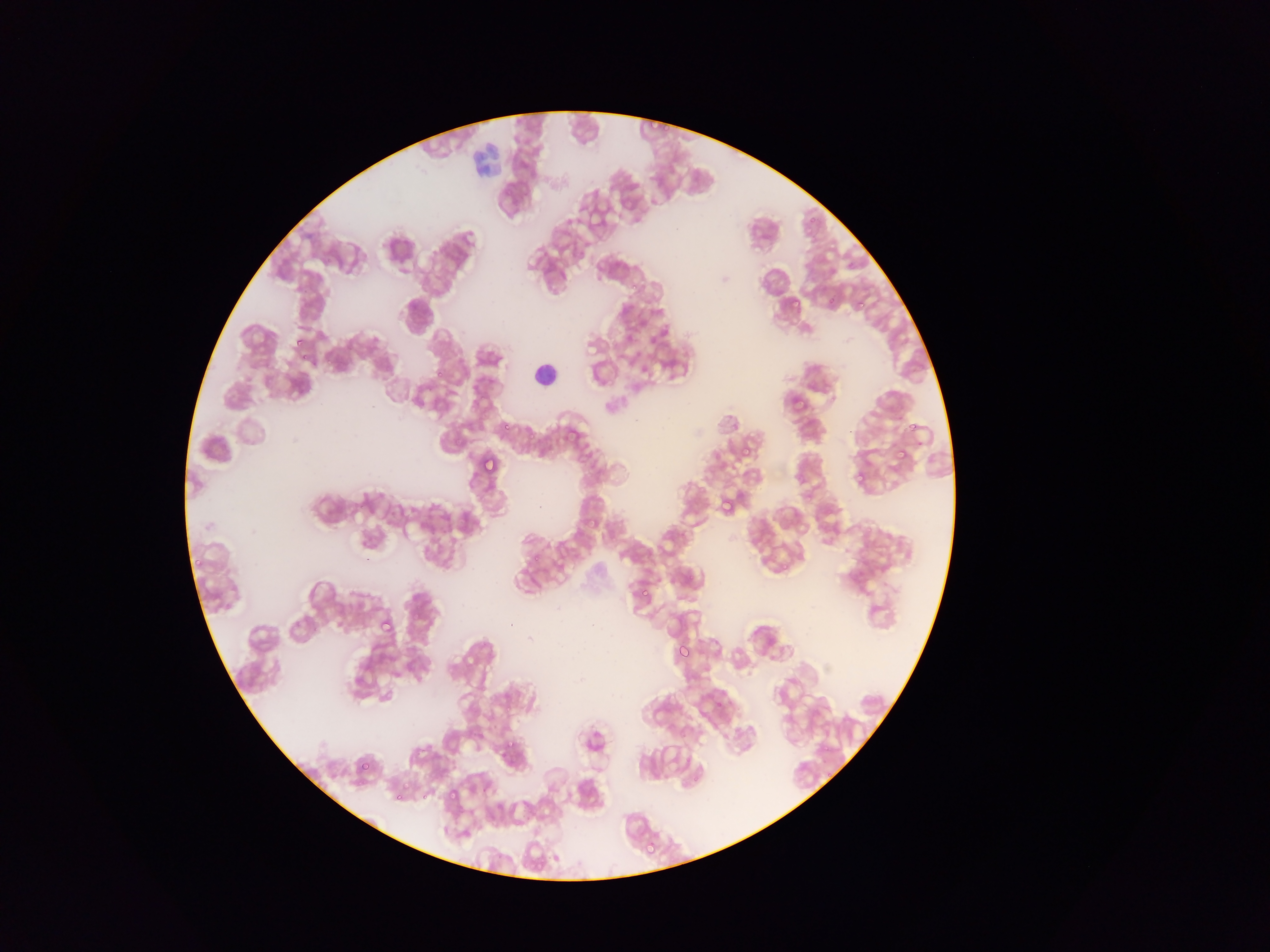
image size = 1270×952 pixels
leukocyte locations = approximate bounding boxes as (left, top, right, bottom) in pixels: (465, 135, 505, 180), (526, 351, 563, 392)
field of view = single
country = Ghana
preparation = thin blood smear
capture = mobile-phone photograph through a microscope
malaria parasite locations = approximate bounding boxes as (left, top, right, bottom) in pixels: (803, 214, 820, 234), (845, 260, 856, 270), (623, 283, 637, 293), (823, 292, 837, 306), (787, 295, 807, 309), (858, 300, 869, 311), (290, 329, 313, 349), (903, 421, 917, 435), (497, 422, 510, 433), (526, 427, 540, 441), (482, 446, 502, 475), (741, 448, 753, 459), (893, 448, 907, 460), (892, 449, 898, 462), (848, 474, 858, 485), (718, 494, 732, 512), (431, 502, 440, 510), (527, 547, 549, 564), (639, 574, 657, 597), (377, 611, 396, 634), (674, 643, 690, 660), (352, 674, 367, 687), (506, 737, 517, 751), (359, 757, 373, 772), (446, 773, 466, 804), (398, 779, 412, 790), (416, 783, 434, 804), (392, 796, 397, 804), (643, 838, 658, 855)